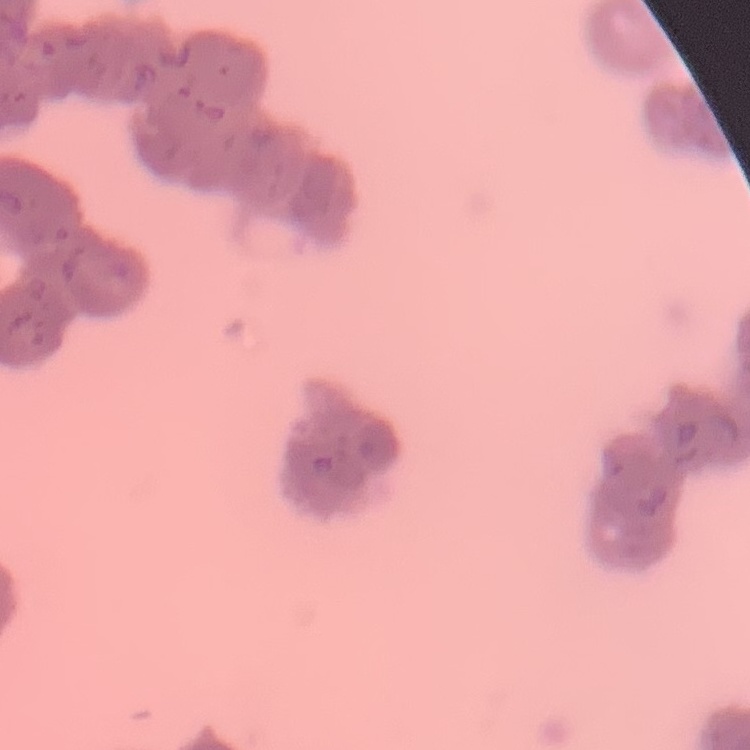
{
  "erythrocyte_morphology": "rouleaux formation",
  "image_type": "one tile cut from a larger photomicrograph",
  "preparation": "thin peripheral smear",
  "stain": "Field's or Giemsa"
}